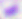
Photomicrograph. Toxoplasma gondii is seen. Captured at 400x magnification.